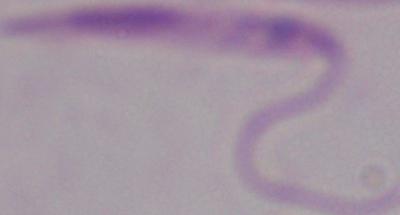

Summary:
  - Magnification: 1000x
  - Modality: photomicrograph
  - Identification: Leishmania